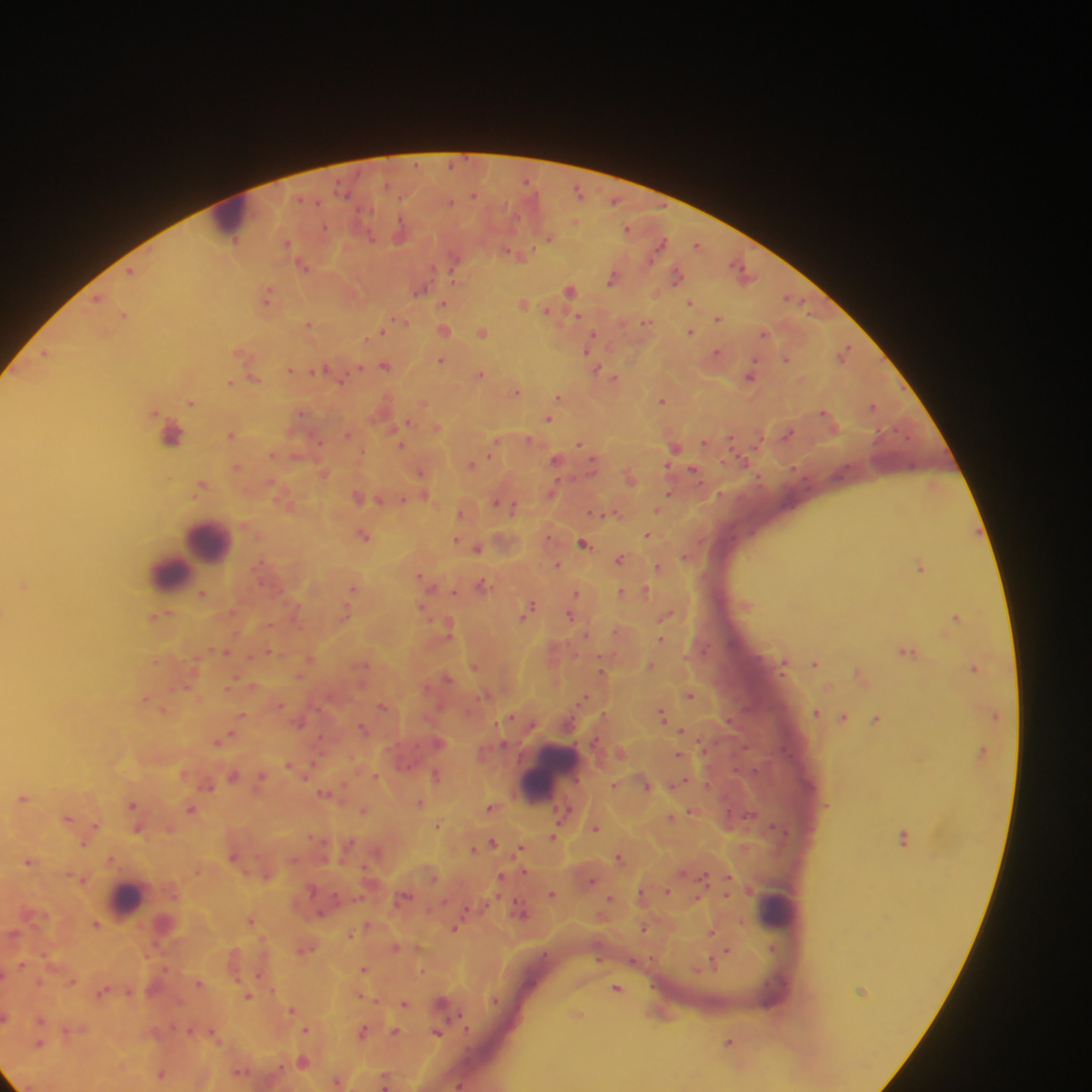
Approximate centers as {x, y} in pixels. Leukocyte locations: {230, 216}, {185, 433}, {201, 545}, {178, 565}, {547, 772}, {127, 899}, {778, 910}. Plasmodium parasite locations: {580, 192}, {473, 195}, {614, 200}, {452, 201}, {628, 229}, {401, 230}, {370, 236}, {548, 238}, {287, 243}, {659, 245}, {698, 245}, {515, 254}, {455, 264}, {303, 265}, {130, 271}, {744, 271}, {677, 274}, {613, 278}, {421, 289}, {570, 289}, {268, 296}, {98, 298}, {790, 298}, {690, 301}, {524, 302}, {443, 303}, {549, 311}, {125, 314}, {577, 317}, {718, 317}, {400, 322}, {647, 322}, {309, 324}, {393, 325}, {444, 329}, {382, 331}, {691, 331}, {482, 332}, {765, 332}, {592, 339}, {588, 347}, {242, 351}, {718, 352}, {845, 352}, {46, 353}, {786, 358}, {441, 360}, {386, 365}, {359, 367}, {323, 368}, {292, 370}, {598, 370}, {479, 373}, {608, 374}, {751, 375}, {343, 377}, {615, 378}, {254, 379}, {230, 383}, {517, 391}, {560, 398}, {663, 400}, {192, 402}, {423, 403}, {873, 405}, {302, 413}, {549, 418}, {409, 421}, {436, 427}, {789, 432}, {349, 433}, {231, 434}, {731, 437}, {529, 438}, {495, 442}, {705, 443}, {401, 444}, {580, 444}, {675, 446}, {272, 454}, {297, 455}, {557, 459}, {472, 463}, {593, 464}, {668, 466}, {237, 467}, {694, 470}, {324, 472}, {421, 472}, {630, 476}, {202, 486}, {552, 492}, {669, 494}, {424, 495}, {358, 497}, {382, 499}, {403, 500}, {289, 501}, {498, 503}, {511, 505}, {657, 508}, {462, 511}, {615, 512}, {596, 513}, {365, 534}, {648, 534}, {457, 540}, {585, 543}, {478, 547}, {687, 557}, {621, 558}, {558, 565}, {658, 566}, {921, 567}, {422, 576}, {428, 582}, {23, 584}, {483, 584}, {355, 588}, {454, 591}, {623, 592}, {636, 592}, {646, 592}, {203, 593}, {576, 593}, {529, 606}, {422, 607}, {234, 611}, {346, 612}, {571, 614}, {160, 615}, {667, 615}, {957, 616}, {270, 624}, {448, 625}, {619, 631}, {662, 639}, {226, 651}, {273, 652}, {908, 652}, {251, 656}, {310, 658}, {157, 660}, {784, 662}, {815, 662}, {362, 665}, {475, 665}, {650, 666}, {974, 668}, {602, 671}, {862, 675}, {300, 676}, {447, 677}, {236, 681}, {187, 687}, {229, 687}, {690, 694}, {147, 698}, {583, 699}, {280, 704}, {384, 705}, {164, 710}, {816, 712}, {663, 714}, {242, 715}, {844, 716}, {510, 717}, {877, 719}, {300, 721}, {364, 728}, {683, 732}, {225, 738}, {219, 740}, {439, 742}, {679, 754}, {289, 764}, {312, 766}, {436, 774}, {234, 775}, {261, 776}, {376, 777}, {208, 784}, {646, 784}, {677, 784}, {615, 785}, {325, 793}, {24, 797}, {420, 803}, {133, 804}, {491, 806}, {191, 809}, {364, 810}, {692, 811}, {69, 817}, {672, 817}, {438, 825}, {95, 826}, {596, 827}, {138, 829}, {554, 836}, {88, 837}, {905, 837}, {493, 842}, {84, 843}, {349, 844}, {474, 848}, {521, 849}, {378, 851}, {235, 856}, {620, 857}, {112, 859}, {30, 860}, {198, 870}, {268, 875}, {704, 876}, {502, 877}, {728, 878}, {82, 879}, {592, 881}, {668, 890}, {552, 894}, {641, 895}, {727, 895}, {404, 897}, {611, 898}, {699, 899}, {521, 910}, {251, 920}, {96, 924}, {368, 925}, {456, 927}, {645, 928}, {712, 931}, {350, 935}, {396, 947}, {306, 948}, {773, 948}, {728, 950}, {599, 958}, {22, 963}, {710, 964}, {700, 966}, {364, 969}, {423, 971}, {261, 974}, {73, 980}, {199, 983}, {618, 988}, {103, 991}, {248, 996}, {362, 996}, {495, 1000}, {405, 1003}, {442, 1003}, {291, 1009}, {576, 1014}, {7, 1017}, {41, 1018}, {306, 1029}, {190, 1030}, {395, 1031}, {363, 1032}, {438, 1032}, {214, 1034}, {40, 1042}, {730, 1042}, {304, 1061}, {240, 1071}, {162, 1074}, {386, 1079}, {339, 1081}, {460, 1084}. Collected in Ghana. Mobile-phone photograph taken through the microscope. Image is 1092×1092 pixels. Thick blood film. Single field of view.